Evaluate for Plasmodium parasites.
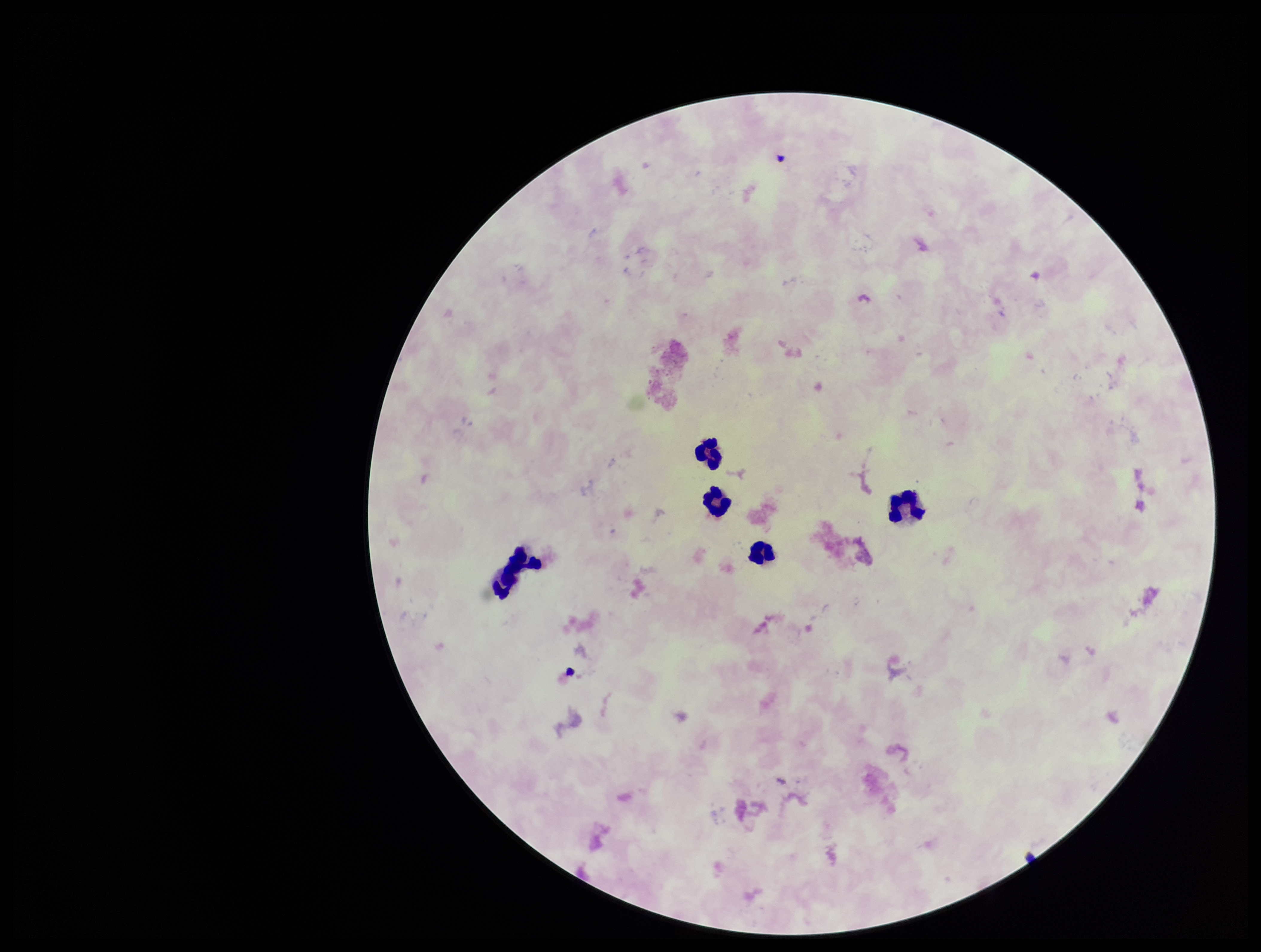

None detected.

parasite count = 0
image size = 1261×952 pixels
patient malaria status = negative
stain = Giemsa
capture = smartphone photograph through the microscope eyepiece
leukocyte count = 5
preparation = thick smear
field of view = one from this slide